Comment on the morphology of the red blood cells.
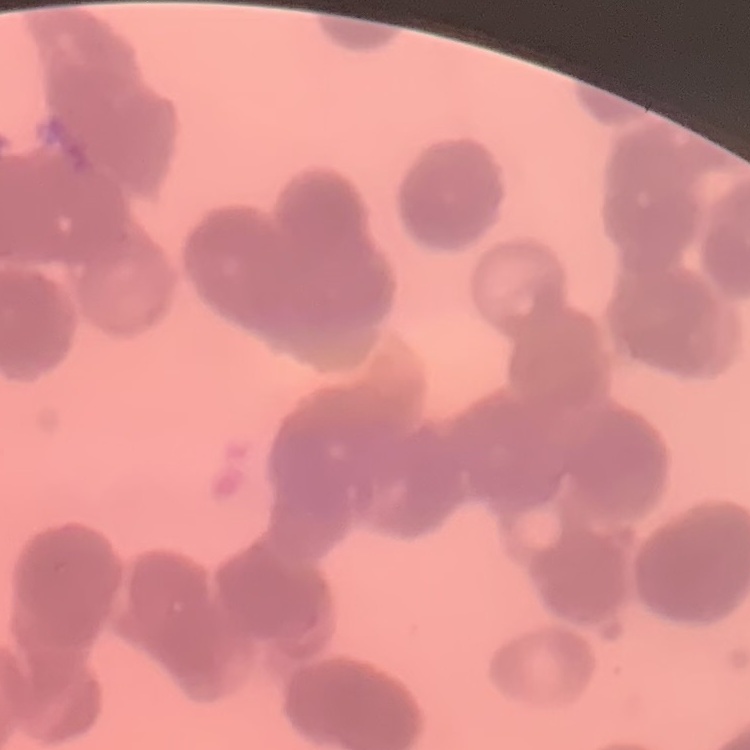

They show rouleaux formation.

Summary:
  - Image type: square crop of a larger photomicrograph
  - Stain: Field's or Giemsa
  - Preparation: thin peripheral smear